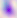
Summary:
  - Identification: Toxoplasma gondii
  - Modality: micrograph
  - Magnification: 400x